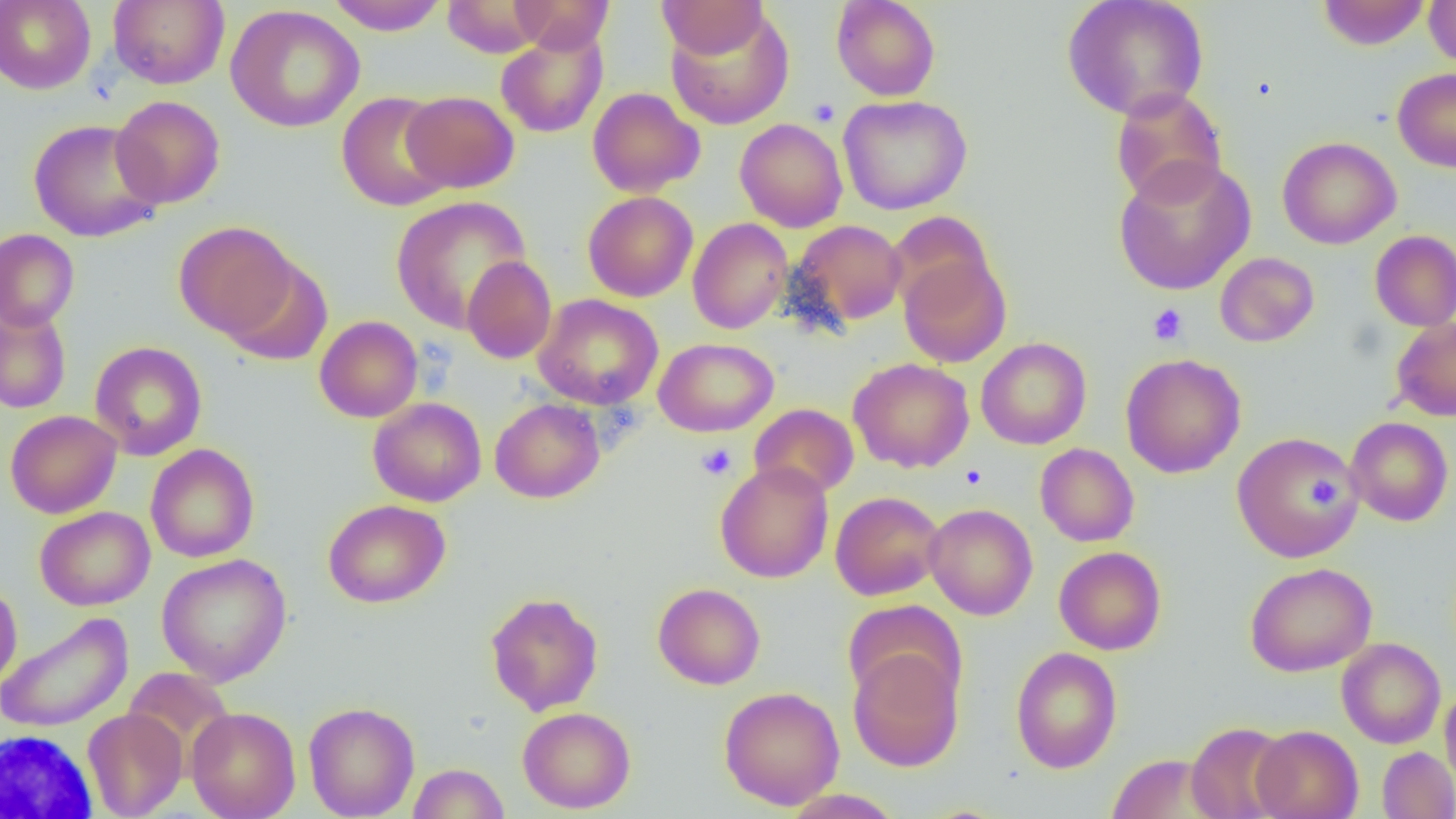

Summary:
  - Coordinate format: approximate bounding boxes as (x1,y1)-(x2,y2) corner pairs in pixels
  - Uninfected red blood cell locations: (0,0)-(96,94), (108,0)-(229,89), (325,0)-(449,35), (441,0)-(544,56), (510,0)-(614,54), (830,0)-(941,101), (1061,0)-(1210,121), (1317,0)-(1430,50), (1423,0)-(1456,69), (657,1)-(768,57), (225,5)-(365,132), (665,7)-(795,131), (495,27)-(608,138), (1392,68)-(1456,172), (587,87)-(705,197), (1110,87)-(1227,206), (337,91)-(454,211), (401,91)-(519,193), (838,94)-(973,215), (111,95)-(225,209), (734,118)-(848,232), (28,119)-(164,242), (1277,136)-(1401,249), (1113,156)-(1256,296), (583,191)-(698,302), (390,195)-(533,333), (885,211)-(996,315), (687,218)-(793,334), (173,220)-(298,340), (790,220)-(907,328), (0,228)-(79,331), (1370,230)-(1456,332), (898,252)-(1012,368), (1215,252)-(1319,347), (220,256)-(333,367), (462,256)-(557,364), (533,294)-(664,409), (0,305)-(72,414), (314,316)-(423,423), (1391,318)-(1456,422), (654,337)-(779,436), (976,337)-(1091,450), (89,341)-(207,460), (1120,353)-(1246,478), (848,357)-(975,473), (368,397)-(486,506), (490,398)-(605,503), (749,403)-(859,499), (5,410)-(121,518), (1345,417)-(1454,526), (1231,431)-(1363,564), (145,443)-(259,563), (1035,443)-(1139,546), (715,461)-(834,583), (830,491)-(945,600), (323,499)-(451,608), (924,503)-(1038,620), (34,506)-(155,610), (1054,546)-(1166,655), (156,553)-(292,686), (1245,562)-(1377,677), (0,580)-(22,689), (653,583)-(765,690), (485,591)-(604,716), (842,599)-(965,710), (0,612)-(133,733), (1336,638)-(1446,748), (1010,646)-(1122,773), (848,648)-(964,772), (1440,683)-(1456,795), (719,686)-(845,810), (303,701)-(419,818), (517,706)-(636,813), (187,707)-(301,819), (82,708)-(187,818), (1185,722)-(1293,819), (1251,725)-(1363,819), (1378,746)-(1456,818), (1106,753)-(1225,818), (406,763)-(510,818), (780,788)-(904,818)
  - White blood cell locations: (1,614)-(129,731), (0,728)-(99,817)
  - Platelet locations: (808,97)-(841,127), (1147,303)-(1188,346), (696,443)-(737,480), (959,464)-(987,490), (1311,470)-(1347,509)
  - Slide-level diagnosis: negative for blood parasites
  - Field of view: single
  - Magnification: 1000x
  - Modality: optical microscopy
  - Image size: 1456×819 pixels
  - Preparation: thin blood film